Assess this cell for malaria.
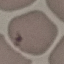
It is uninfected.

preparation = thin smear
capture = smartphone through the microscope eyepiece
stain = Giemsa
image type = cell patch, automatically extracted from a larger field of view and resized to 64 × 64 pixels